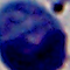
modality = micrograph
magnification = 1000x
identification = leukocyte